Give the position of every malaria parasite.
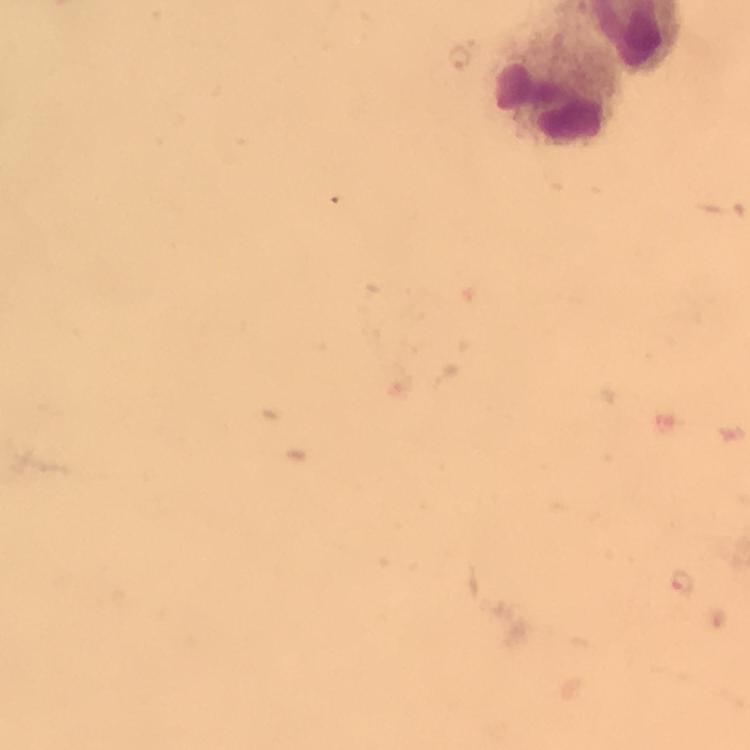
Approximate centers as [x, y] in pixels.
Malaria parasites: [684, 585].

Leukocyte locations: [563, 89]. Immersion oil applied. Thick blood smear. Cropped region of a single field of view. 100x magnification. Photographed through the microscope with a smartphone camera. From a diagnostic examination for malaria. Image is 750×750 pixels. Giemsa stain.